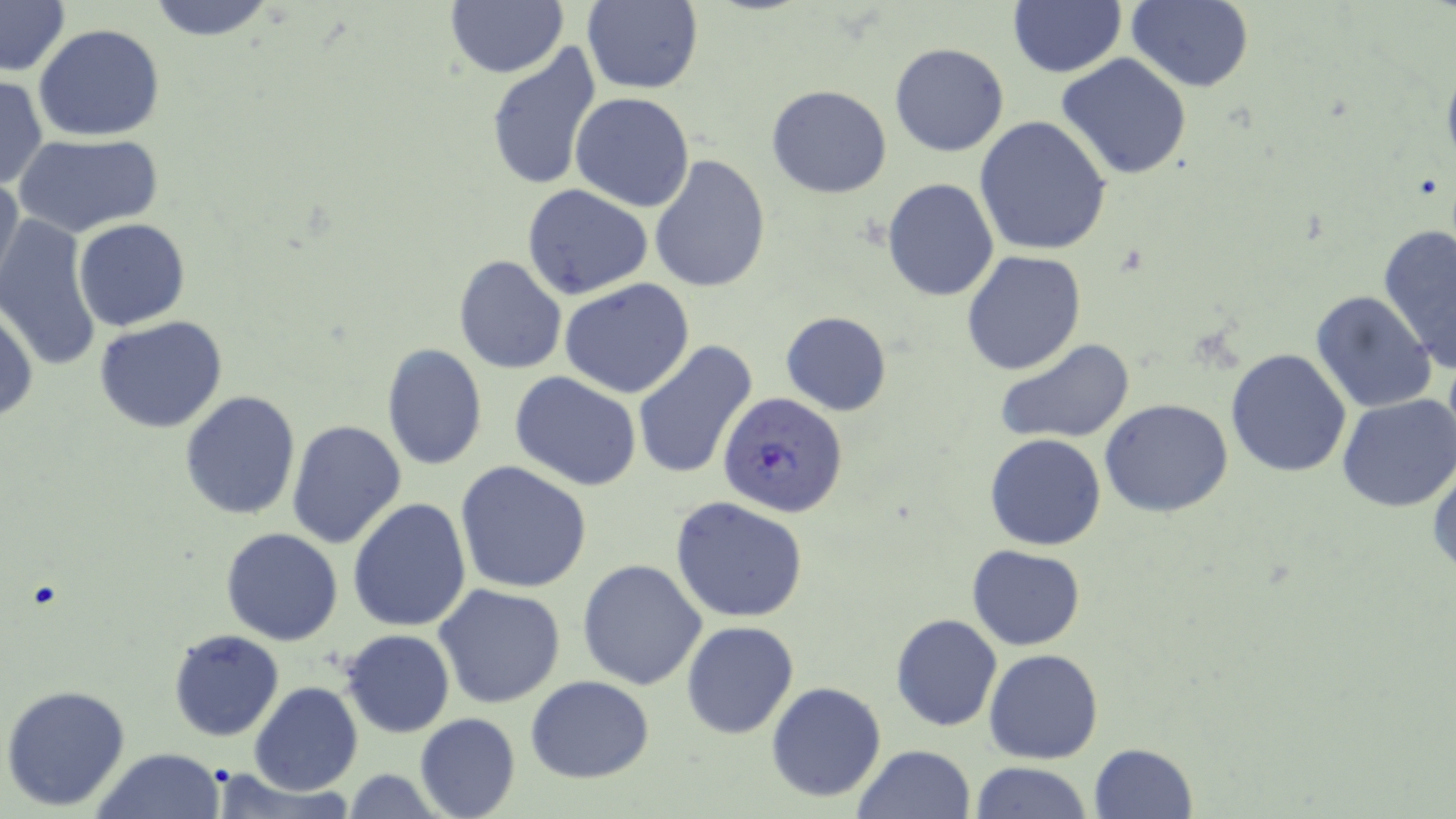
Summary:
  - Coordinate format: approximate bounding boxes as [x1, y1, x2, y2] in pixels
  - Uninfected red blood cell locations: [145, 0, 280, 40], [444, 0, 568, 78], [1126, 0, 1254, 93], [0, 1, 72, 76], [579, 1, 704, 93], [1008, 1, 1126, 77], [33, 24, 165, 142], [485, 42, 601, 192], [889, 42, 1009, 157], [1056, 53, 1193, 180], [0, 75, 47, 189], [767, 85, 892, 198], [569, 91, 694, 210], [974, 116, 1114, 257], [16, 134, 164, 238], [648, 155, 771, 294], [0, 170, 25, 293], [882, 179, 999, 301], [521, 183, 653, 301], [1, 214, 103, 373], [73, 219, 191, 331], [1378, 224, 1456, 373], [961, 249, 1086, 375], [454, 254, 567, 375], [560, 278, 695, 399], [1310, 289, 1437, 413], [0, 302, 37, 423], [780, 311, 890, 416], [94, 315, 228, 433], [995, 339, 1136, 444], [629, 340, 758, 481], [381, 342, 488, 471], [1225, 349, 1354, 479], [509, 372, 642, 493], [179, 389, 303, 521], [1336, 393, 1456, 512], [1101, 399, 1234, 518], [286, 420, 406, 548], [985, 433, 1106, 551], [1428, 456, 1456, 580], [453, 461, 593, 594], [669, 496, 810, 624], [348, 499, 472, 632], [222, 526, 343, 646], [968, 545, 1085, 650], [576, 559, 707, 690], [434, 584, 567, 710], [891, 613, 1002, 731], [681, 620, 799, 738], [169, 629, 284, 741], [340, 629, 454, 737], [985, 648, 1103, 764], [525, 673, 656, 783], [247, 682, 363, 797], [767, 682, 887, 803], [1, 684, 132, 813], [414, 712, 521, 819], [1086, 743, 1198, 819], [852, 744, 977, 819], [94, 748, 224, 819], [970, 761, 1091, 818], [338, 767, 449, 819]
  - Plasmodium falciparum-infected red blood cell locations: [718, 391, 849, 517]
  - Slide-level diagnosis: Plasmodium falciparum
  - Magnification: 1000x
  - Image size: 1456×819 pixels
  - Stain: May-Grünwald-Giemsa
  - Modality: optical microscopy
  - Preparation: thin blood smear
  - Field of view: single